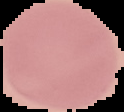

Segmented cell region on a black background. From a thin blood film. Malaria status: uninfected. Image is 124×112 pixels.